Assess this cell for malaria.
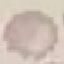
It is uninfected.

Summary:
  - Capture: smartphone through the microscope eyepiece
  - Image type: automatically extracted cell patch, resized to 64 × 64 pixels
  - Preparation: thin blood film
  - Stain: Giemsa